Classify this cell by malaria status.
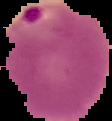

Parasitized.

Cell region segmented out of the field of view; the surrounding area is masked to black. Image is 112×121 pixels. From a thin blood smear.